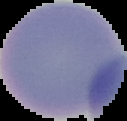
From a thin blood smear. Image is 127×121 pixels. Malaria status: uninfected. Segmented cell region on a black background.